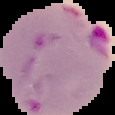

image_type: segmented cell region on a black background
preparation: thin blood film
image_size: 115×115 pixels
result: malaria parasites identified